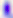
identification: Toxoplasma gondii
magnification: 400x
modality: micrograph